Describe the morphology of the red blood cells.
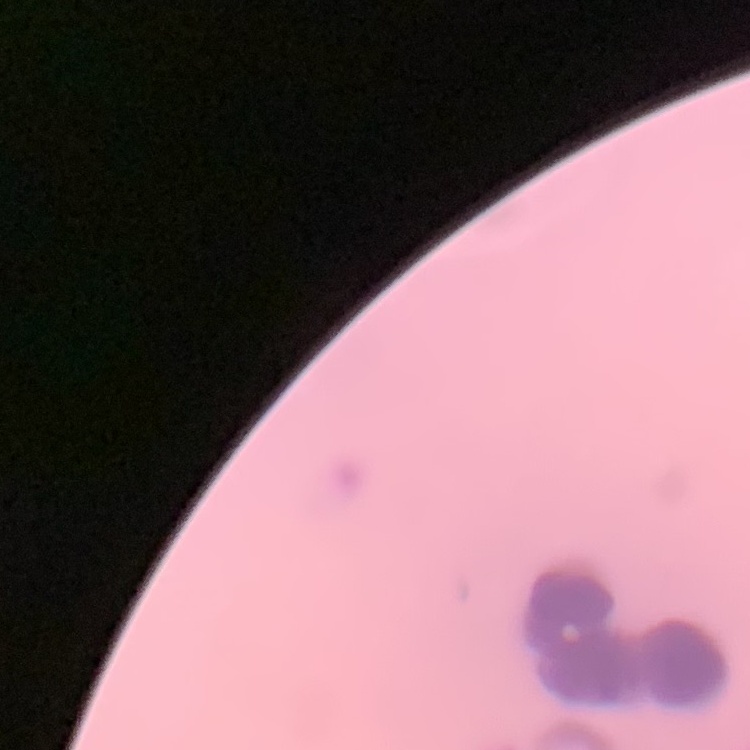
Rouleaux formation.

image type = one tile cut from a larger photomicrograph
preparation = thin blood smear
stain = Field's or Giemsa